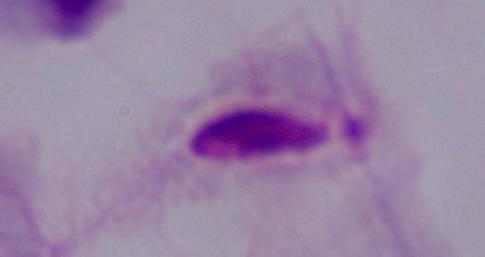

Summary:
  - Modality: micrograph
  - Identification: trichomonad
  - Magnification: 1000x